Locate every uninfected red blood cell.
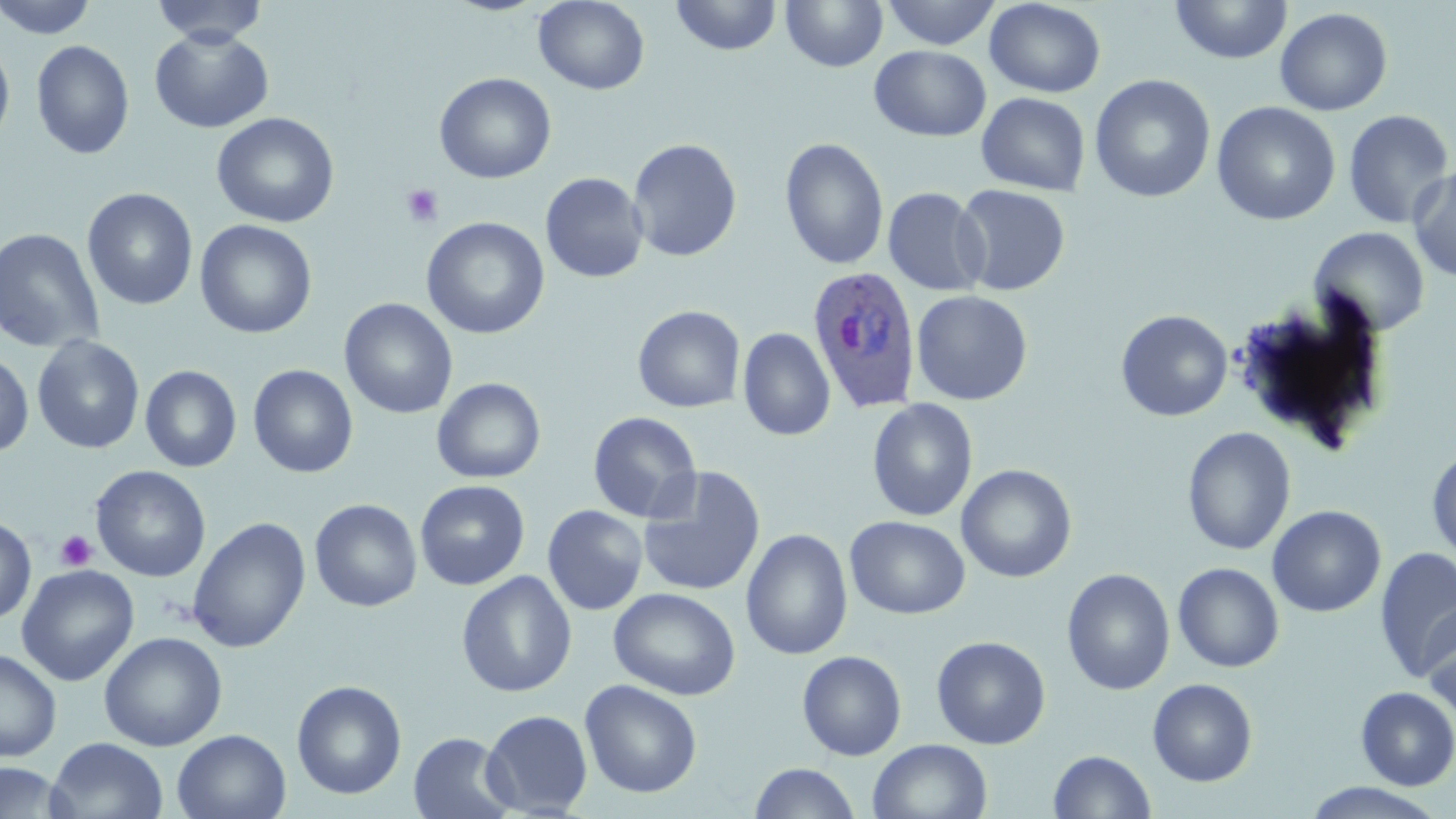

Approximate bounding boxes as named x1/y1/x2/y2 corners in pixels.
Uninfected red blood cells: (x1=0, y1=0, x2=99, y2=39), (x1=150, y1=0, x2=268, y2=46), (x1=670, y1=0, x2=783, y2=56), (x1=781, y1=0, x2=888, y2=71), (x1=880, y1=0, x2=1001, y2=50), (x1=1169, y1=0, x2=1292, y2=64), (x1=533, y1=1, x2=650, y2=95), (x1=984, y1=1, x2=1106, y2=98), (x1=1274, y1=7, x2=1393, y2=116), (x1=149, y1=27, x2=273, y2=134), (x1=0, y1=39, x2=15, y2=150), (x1=31, y1=40, x2=134, y2=160), (x1=869, y1=45, x2=992, y2=141), (x1=434, y1=72, x2=557, y2=184), (x1=1089, y1=74, x2=1216, y2=203), (x1=976, y1=92, x2=1090, y2=197), (x1=1211, y1=101, x2=1341, y2=226), (x1=1343, y1=109, x2=1454, y2=229), (x1=211, y1=112, x2=339, y2=228), (x1=780, y1=137, x2=889, y2=271), (x1=627, y1=138, x2=742, y2=262), (x1=1408, y1=165, x2=1456, y2=283), (x1=540, y1=172, x2=649, y2=284), (x1=953, y1=184, x2=1071, y2=296), (x1=883, y1=187, x2=990, y2=296), (x1=82, y1=188, x2=198, y2=310), (x1=421, y1=217, x2=550, y2=340), (x1=194, y1=219, x2=318, y2=340), (x1=0, y1=227, x2=105, y2=353), (x1=1309, y1=227, x2=1430, y2=337), (x1=911, y1=290, x2=1033, y2=406), (x1=339, y1=298, x2=457, y2=419), (x1=632, y1=305, x2=745, y2=413), (x1=1116, y1=309, x2=1233, y2=421), (x1=738, y1=327, x2=836, y2=442), (x1=32, y1=336, x2=145, y2=454), (x1=0, y1=352, x2=34, y2=458), (x1=247, y1=364, x2=358, y2=478), (x1=140, y1=365, x2=242, y2=473), (x1=432, y1=377, x2=546, y2=484), (x1=866, y1=398, x2=978, y2=522), (x1=588, y1=411, x2=701, y2=523), (x1=1182, y1=427, x2=1296, y2=556), (x1=1427, y1=448, x2=1456, y2=565), (x1=956, y1=464, x2=1077, y2=583), (x1=90, y1=465, x2=211, y2=582), (x1=638, y1=466, x2=766, y2=597), (x1=415, y1=479, x2=530, y2=590), (x1=309, y1=498, x2=422, y2=612), (x1=1266, y1=504, x2=1386, y2=617), (x1=542, y1=505, x2=648, y2=616), (x1=0, y1=516, x2=37, y2=625), (x1=845, y1=516, x2=970, y2=620), (x1=187, y1=517, x2=311, y2=653), (x1=741, y1=528, x2=853, y2=660), (x1=1374, y1=547, x2=1456, y2=682), (x1=1173, y1=562, x2=1284, y2=672), (x1=16, y1=564, x2=139, y2=686), (x1=1062, y1=568, x2=1175, y2=695), (x1=456, y1=570, x2=577, y2=697), (x1=608, y1=587, x2=741, y2=701), (x1=1421, y1=604, x2=1456, y2=720), (x1=99, y1=631, x2=227, y2=752), (x1=931, y1=635, x2=1051, y2=749), (x1=0, y1=648, x2=61, y2=762), (x1=797, y1=650, x2=907, y2=761), (x1=1147, y1=678, x2=1258, y2=786), (x1=580, y1=679, x2=702, y2=798), (x1=291, y1=680, x2=407, y2=800), (x1=1355, y1=687, x2=1456, y2=790), (x1=481, y1=709, x2=593, y2=817), (x1=172, y1=729, x2=291, y2=818), (x1=408, y1=731, x2=516, y2=819), (x1=46, y1=737, x2=168, y2=819), (x1=868, y1=738, x2=992, y2=819), (x1=1048, y1=750, x2=1156, y2=818), (x1=0, y1=762, x2=73, y2=818), (x1=749, y1=763, x2=860, y2=819), (x1=1302, y1=782, x2=1448, y2=818).

Summary:
  - Platelet locations: (x1=400, y1=184, x2=443, y2=228), (x1=55, y1=530, x2=97, y2=571)
  - Plasmodium ovale-infected red blood cell locations: (x1=806, y1=265, x2=922, y2=412)
  - Slide-level diagnosis: Plasmodium ovale
  - Magnification: 1000x
  - Modality: optical microscopy
  - Stain: May-Grünwald-Giemsa
  - Image size: 1456×819 pixels
  - Preparation: thin blood film
  - Field of view: one of a larger specimen